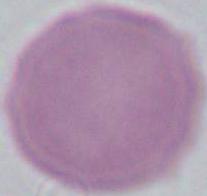 Captured at 1000x magnification. An erythrocyte is seen. Photomicrograph.